Name the cell type shown.
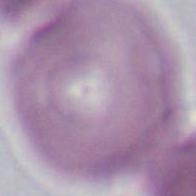
An erythrocyte.

1000x magnification. Micrograph.